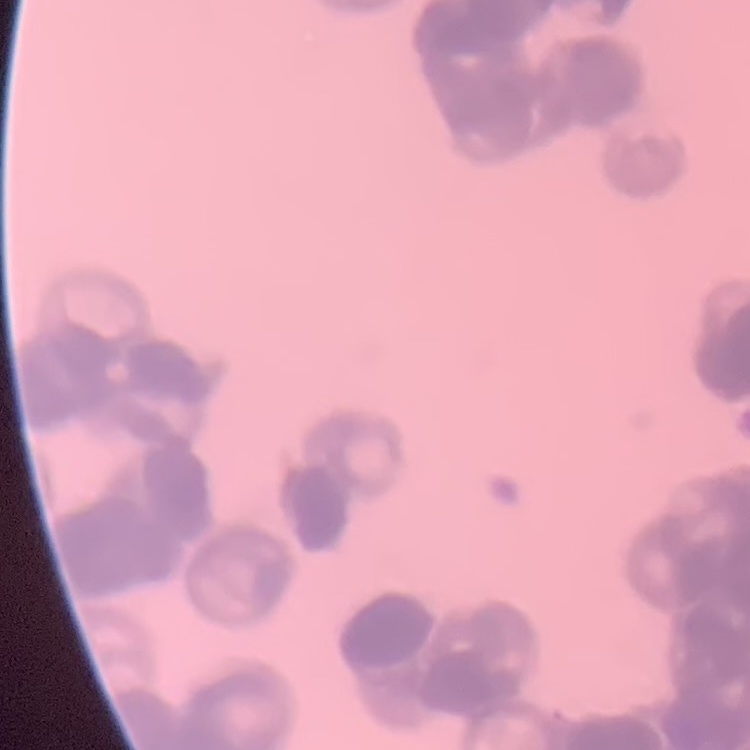

Summary:
  - Erythrocyte morphology: rouleaux formation
  - Image type: one tile cut from a larger photomicrograph
  - Stain: Field's or Giemsa
  - Preparation: thin blood film